Name the parasite shown.
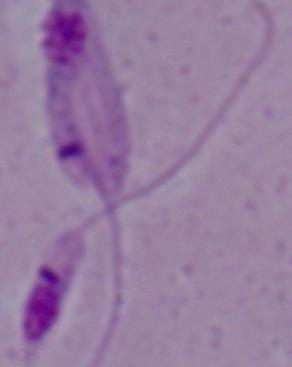
This is Leishmania.

1000x magnification. Micrograph.